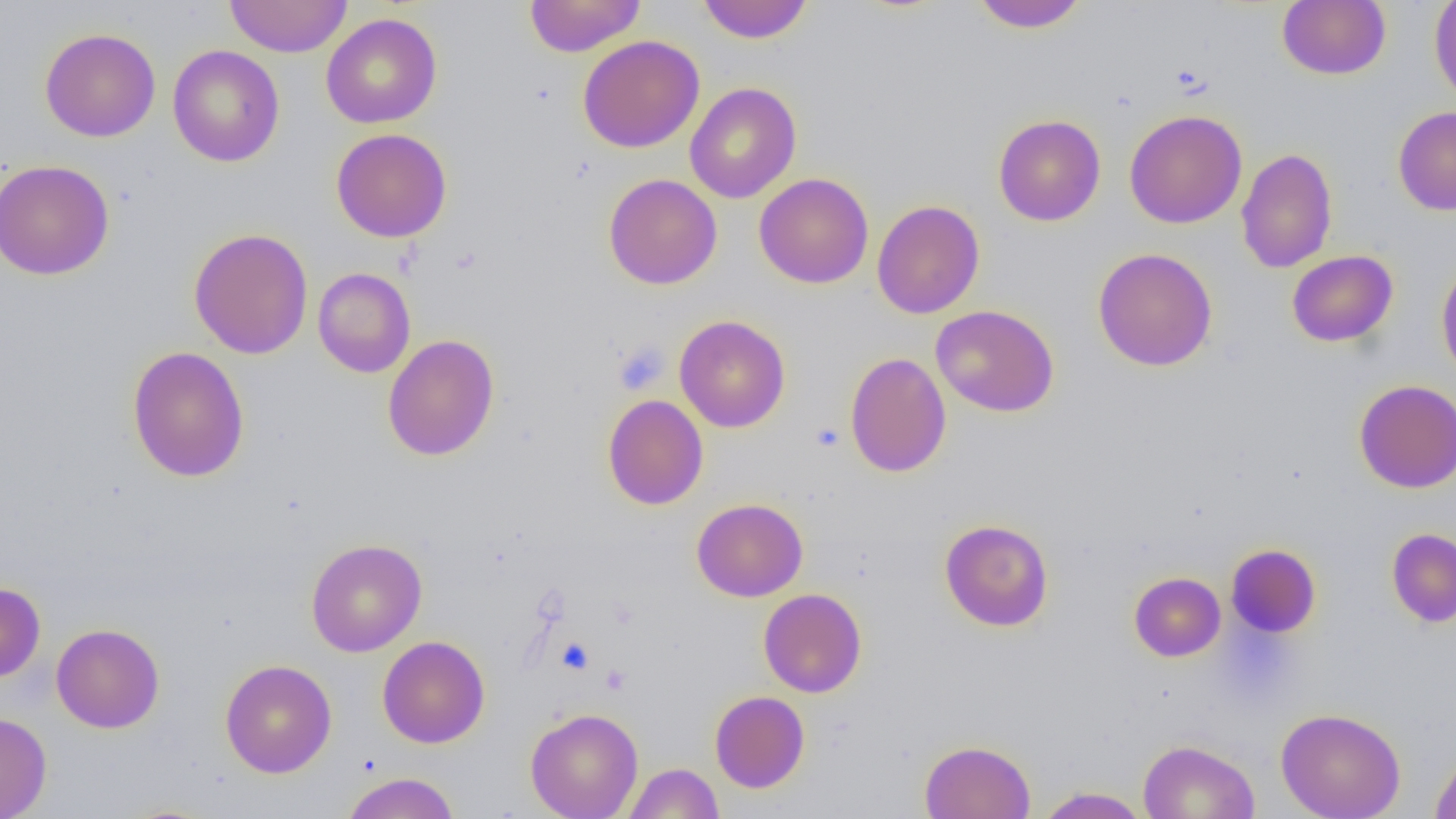 Approximate bounding boxes as (x1,y1)-(x2,y2) corner pairs in pixels. Platelet locations: (613,340)-(669,395), (811,422)-(845,451), (556,636)-(595,674), (600,664)-(631,695). Uninfected red blood cell locations: (224,0)-(352,58), (524,0)-(646,57), (697,0)-(813,44), (1277,0)-(1391,80), (1429,0)-(1456,106), (969,1)-(1089,32), (321,12)-(442,129), (39,27)-(161,142), (577,35)-(705,153), (168,45)-(285,167), (684,82)-(801,204), (1393,106)-(1456,216), (1124,109)-(1247,229), (993,114)-(1106,226), (331,128)-(452,243), (1236,148)-(1337,273), (0,159)-(114,280), (754,173)-(874,289), (604,174)-(722,290), (871,200)-(985,319), (188,227)-(313,360), (1093,247)-(1218,371), (1287,250)-(1398,347), (1436,259)-(1456,382), (312,267)-(416,378), (931,305)-(1060,417), (674,315)-(790,432), (382,334)-(499,461), (126,346)-(250,482), (844,352)-(952,478), (1354,379)-(1456,492), (602,394)-(708,510), (692,498)-(808,602), (939,519)-(1054,632), (1386,528)-(1456,628), (306,538)-(427,657), (1226,544)-(1320,638), (1129,572)-(1226,661), (0,582)-(45,682), (758,588)-(867,698), (51,623)-(165,733), (377,635)-(490,748), (220,659)-(337,778), (710,690)-(810,793), (525,707)-(644,818), (1276,707)-(1406,819), (0,712)-(52,818), (1138,739)-(1260,819), (919,740)-(1036,819), (1430,749)-(1456,819), (623,763)-(724,819), (341,771)-(461,819), (1035,786)-(1151,818). Slide-level diagnosis: negative for blood parasites. Single field of view. 1000x magnification. Optical microscopy. Image is 1456×819 pixels. Thin blood smear.